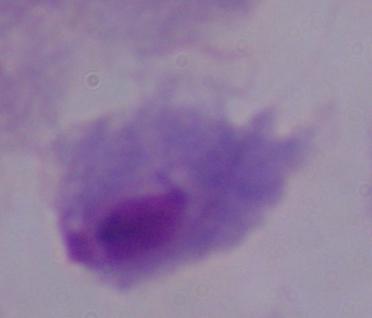

magnification: 1000x
identification: trichomonad
modality: micrograph